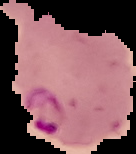
preparation: thin blood film
image_size: 136×154 pixels
malaria_status: parasitized
image_type: segmented cell region on a black background